Give the extent of all uninfected red blood cells.
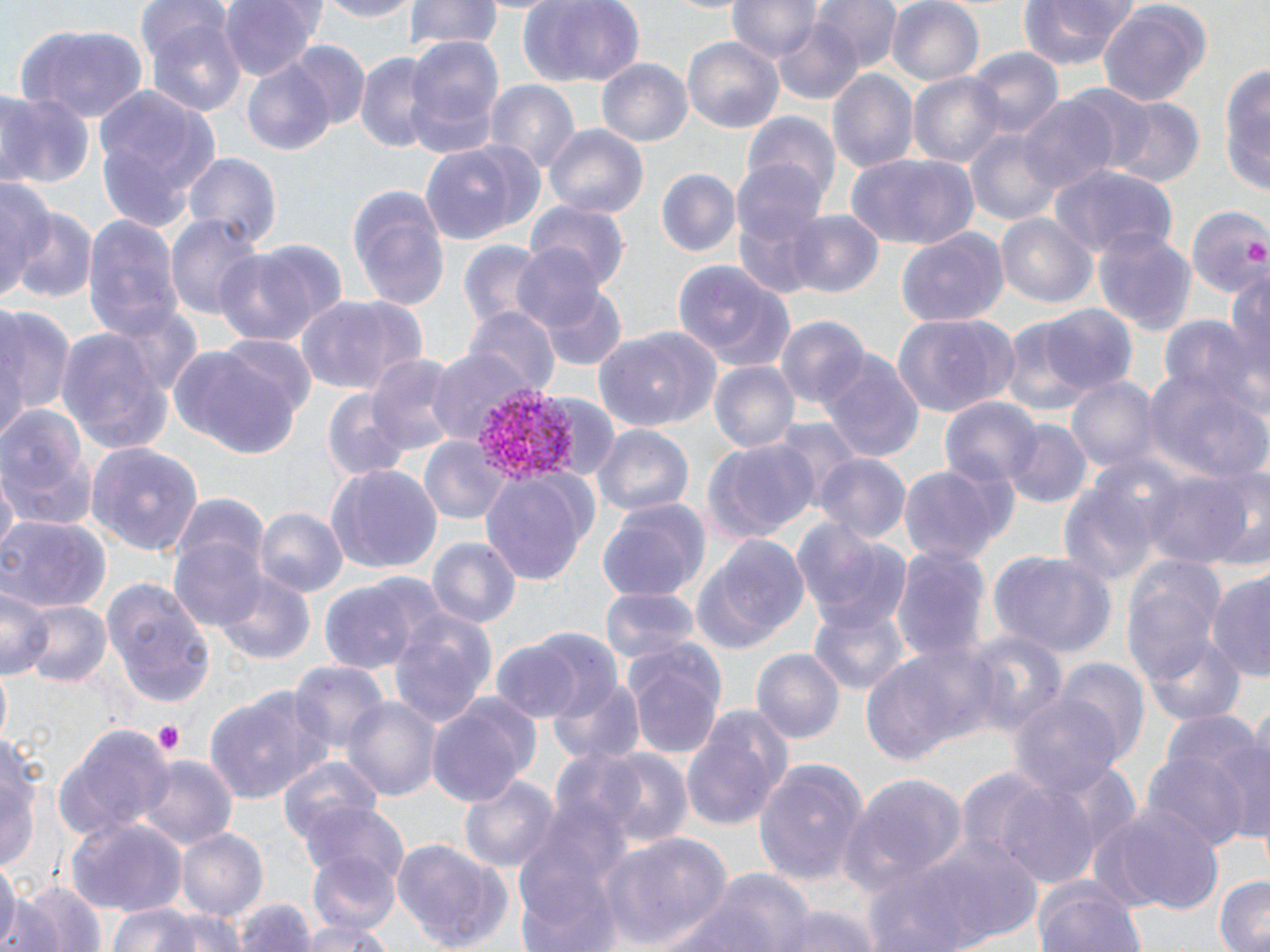

Approximate bounding boxes as [x1, y1, x2, y2] in pixels.
Uninfected red blood cells: [136, 0, 234, 80], [220, 0, 320, 81], [313, 0, 426, 22], [404, 0, 503, 53], [516, 0, 647, 86], [812, 0, 905, 73], [885, 0, 985, 86], [1016, 0, 1138, 72], [1096, 0, 1210, 111], [728, 1, 823, 64], [768, 14, 869, 108], [146, 18, 246, 119], [17, 25, 148, 121], [402, 35, 505, 162], [682, 35, 784, 134], [281, 42, 371, 136], [965, 47, 1065, 139], [356, 52, 437, 156], [596, 60, 692, 149], [1218, 60, 1267, 197], [244, 62, 334, 154], [828, 68, 918, 175], [909, 71, 1006, 170], [482, 78, 581, 178], [91, 83, 220, 236], [0, 92, 92, 189], [1018, 97, 1118, 195], [1102, 98, 1203, 187], [742, 109, 841, 207], [545, 125, 648, 222], [967, 127, 1061, 226], [421, 138, 544, 247], [846, 154, 978, 250], [185, 155, 279, 250], [735, 157, 832, 249], [1048, 164, 1178, 262], [656, 168, 740, 259], [0, 176, 58, 300], [347, 182, 450, 309], [528, 199, 634, 292], [1188, 207, 1270, 295], [12, 208, 97, 304], [787, 209, 883, 296], [995, 213, 1097, 310], [166, 214, 265, 323], [82, 217, 182, 344], [1092, 226, 1197, 337], [895, 227, 1007, 328], [456, 239, 548, 334], [214, 240, 344, 347], [513, 243, 608, 335], [674, 260, 797, 373], [1226, 266, 1270, 390], [540, 286, 626, 371], [292, 295, 422, 397], [1039, 303, 1138, 394], [0, 305, 73, 429], [467, 309, 559, 402], [891, 313, 1020, 419], [776, 315, 868, 408], [1161, 315, 1264, 415], [999, 320, 1095, 418], [57, 326, 178, 454], [595, 327, 721, 432], [215, 336, 316, 422], [169, 343, 308, 456], [424, 348, 533, 445], [818, 349, 926, 465], [365, 354, 465, 459], [709, 361, 799, 455], [1143, 369, 1267, 486], [1066, 376, 1158, 474], [318, 387, 418, 486], [532, 392, 621, 483], [941, 398, 1040, 489], [0, 406, 99, 531], [769, 418, 862, 513], [1001, 419, 1094, 509], [593, 425, 691, 516], [419, 437, 511, 526], [702, 439, 816, 544], [88, 442, 202, 556], [815, 453, 910, 547], [896, 461, 1014, 570], [326, 463, 442, 575], [2, 467, 19, 563], [1146, 470, 1256, 571], [479, 471, 592, 588], [1057, 482, 1162, 592], [171, 492, 270, 583], [598, 499, 711, 599], [255, 508, 346, 598], [0, 515, 112, 614], [792, 518, 911, 634], [168, 533, 268, 633], [695, 535, 812, 651], [427, 537, 521, 631], [890, 545, 991, 666], [988, 549, 1118, 657], [1119, 556, 1232, 702], [215, 571, 315, 666], [1207, 572, 1270, 684], [101, 578, 214, 713], [320, 580, 420, 675], [0, 584, 49, 680], [599, 586, 699, 669], [17, 599, 113, 689], [808, 602, 912, 697], [388, 613, 496, 734], [963, 626, 1066, 738], [521, 629, 622, 722], [622, 638, 726, 761], [491, 639, 583, 724], [862, 639, 991, 767], [753, 648, 845, 744], [292, 658, 386, 757], [1055, 658, 1149, 765], [548, 676, 644, 767], [203, 685, 334, 805], [1008, 693, 1122, 796], [342, 695, 441, 803], [426, 697, 534, 809], [678, 699, 793, 833], [1167, 714, 1270, 837], [0, 723, 43, 879], [55, 726, 171, 841], [1223, 734, 1270, 850], [594, 749, 693, 848], [1144, 750, 1252, 854], [136, 756, 238, 856], [277, 759, 383, 853], [753, 759, 870, 886], [849, 772, 970, 892], [458, 773, 561, 873], [986, 775, 1108, 890], [513, 792, 633, 947], [297, 800, 409, 889], [1091, 803, 1225, 914], [66, 816, 189, 916], [177, 829, 266, 920], [875, 831, 1041, 952], [593, 833, 732, 951], [392, 838, 512, 952], [0, 852, 20, 951], [307, 853, 402, 936], [671, 870, 825, 952], [1032, 875, 1143, 952], [2, 876, 48, 952], [1213, 876, 1270, 952], [14, 880, 107, 952], [235, 896, 318, 952], [104, 901, 221, 952], [771, 903, 885, 952], [295, 916, 392, 951].

slide-level diagnosis = Plasmodium vivax
modality = optical microscopy
platelet locations = approximate bounding boxes as [x1, y1, x2, y2] in pixels: [1246, 241, 1269, 268], [152, 721, 187, 754]
field of view = single
Plasmodium vivax-infected red blood cell locations = approximate bounding boxes as [x1, y1, x2, y2] in pixels: [476, 384, 584, 484]
preparation = thin blood smear
image size = 1270×952 pixels
stain = May-Grünwald-Giemsa
magnification = 1000x